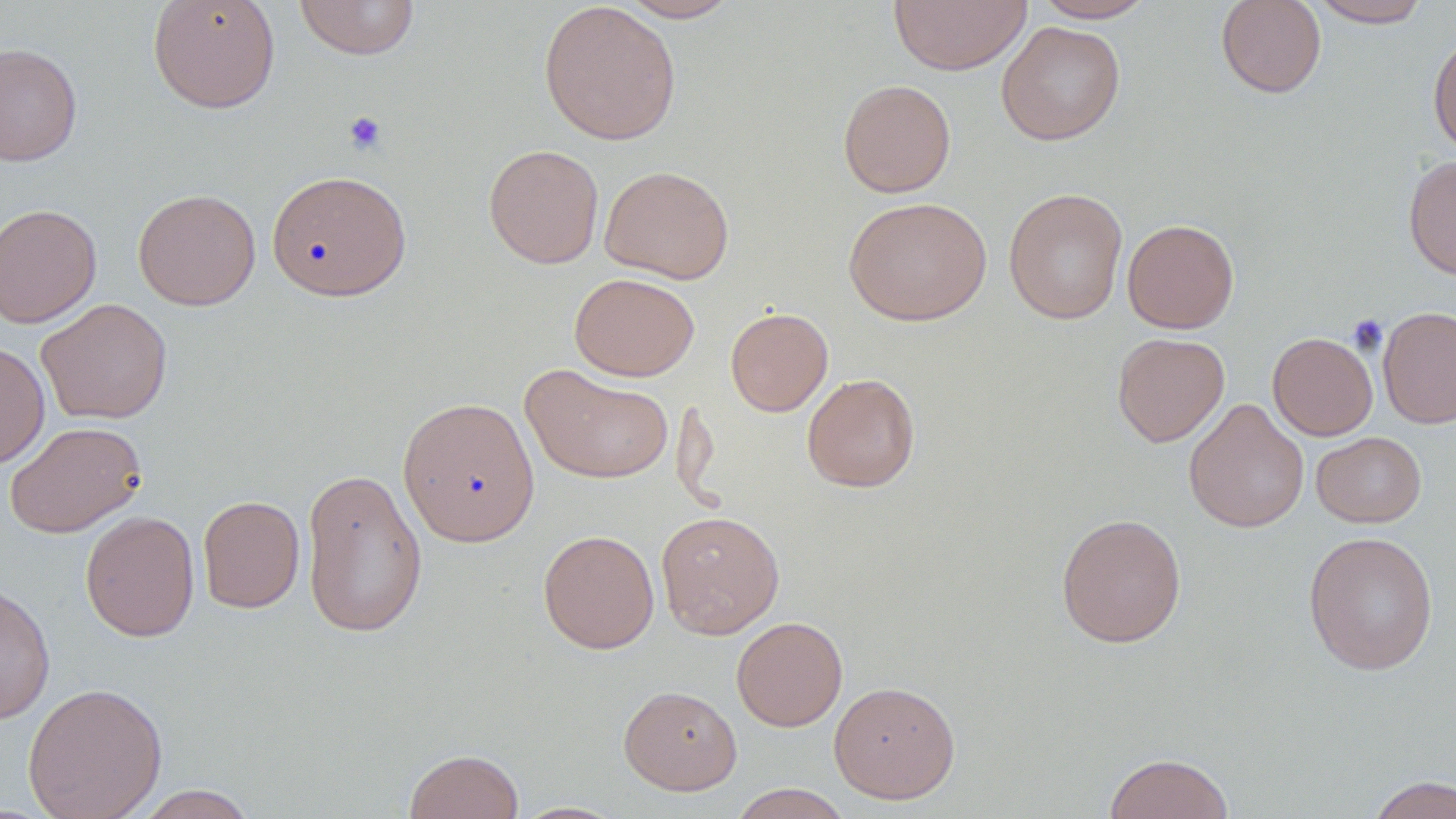
Approximate bounding boxes as (x1, y1, x2, y2) in pixels. Platelet locations: (342, 110, 388, 156), (1347, 315, 1388, 355). Uninfected red blood cell locations: (147, 0, 281, 113), (293, 0, 421, 60), (1033, 0, 1157, 22), (1215, 0, 1327, 98), (1309, 0, 1432, 27), (538, 1, 682, 146), (616, 1, 741, 22), (889, 1, 1031, 75), (996, 21, 1126, 145), (1428, 31, 1456, 159), (0, 41, 83, 167), (837, 79, 956, 198), (483, 144, 605, 269), (1403, 155, 1456, 281), (600, 165, 734, 284), (266, 170, 412, 301), (1003, 187, 1128, 324), (133, 188, 261, 310), (842, 195, 993, 326), (0, 203, 102, 329), (1122, 218, 1239, 333), (569, 272, 700, 381), (36, 299, 173, 424), (1378, 306, 1456, 429), (725, 307, 834, 416), (1112, 332, 1229, 447), (1267, 332, 1378, 440), (0, 340, 50, 469), (520, 363, 674, 484), (802, 373, 921, 492), (397, 396, 540, 547), (1183, 398, 1309, 533), (4, 421, 146, 538), (1311, 431, 1427, 528), (301, 467, 428, 639), (198, 495, 305, 613), (80, 510, 200, 642), (656, 510, 785, 639), (1055, 512, 1187, 648), (537, 529, 660, 654), (1302, 530, 1439, 676), (0, 581, 56, 724), (732, 616, 848, 732), (829, 680, 961, 803), (22, 681, 168, 819), (618, 685, 742, 795), (404, 748, 524, 819), (1103, 752, 1234, 818), (1365, 775, 1456, 819), (728, 783, 853, 819), (132, 785, 259, 818), (510, 801, 628, 818). Slide-level diagnosis: negative for blood parasites. Single field of view. May-Grünwald-Giemsa-stained preparation. Image is 1456×819 pixels. 1000x magnification. Thin blood smear. Light microscopy.